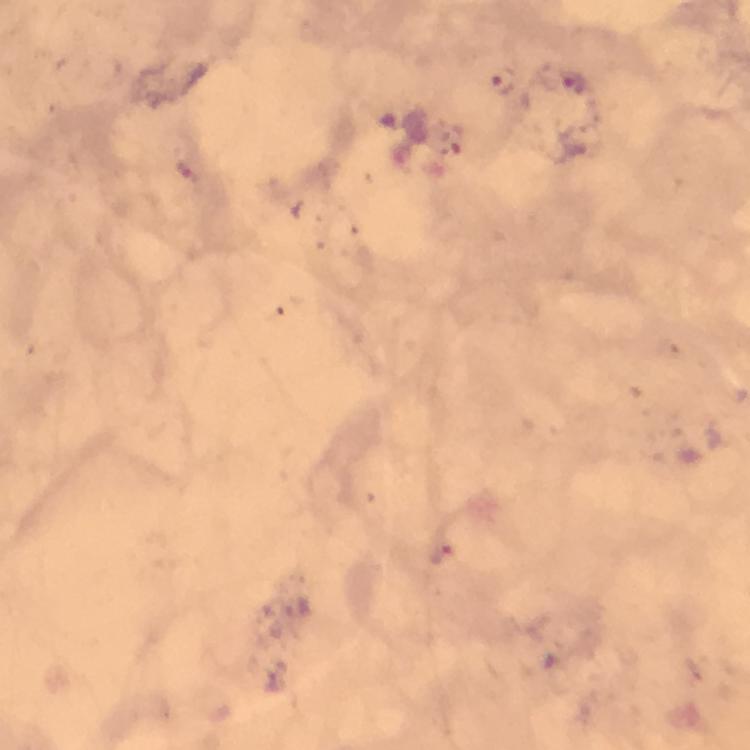
{
  "magnification": "100x",
  "capture": "smartphone mounted on the microscope",
  "context": "from a diagnostic examination for malaria",
  "stain": "Giemsa",
  "image_size": "750×750 pixels",
  "immersion_oil": "applied",
  "cropped_from": "one field of view",
  "preparation": "thick blood film",
  "plasmodium_parasite_locations": "approximate object centers, in pixels from the top-left corner: (x=571, y=80), (x=503, y=83), (x=443, y=556)"
}